Classify this cell by malaria status.
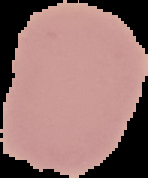
Uninfected.

Cell region segmented out of the field of view; the surrounding area is masked to black. Image is 148×178 pixels. From a thin blood smear.